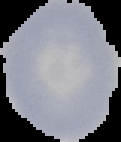
{
  "image_type": "cell region segmented out of the field of view; surrounding area masked to black",
  "image_size": "121×142 pixels",
  "preparation": "thin blood smear",
  "result": "negative for Plasmodium parasites"
}